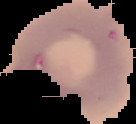
Summary:
  - Image type: cell region segmented out of the field of view; surrounding area masked to black
  - Preparation: thin blood smear
  - Image size: 136×124 pixels
  - Result: no malaria parasites seen